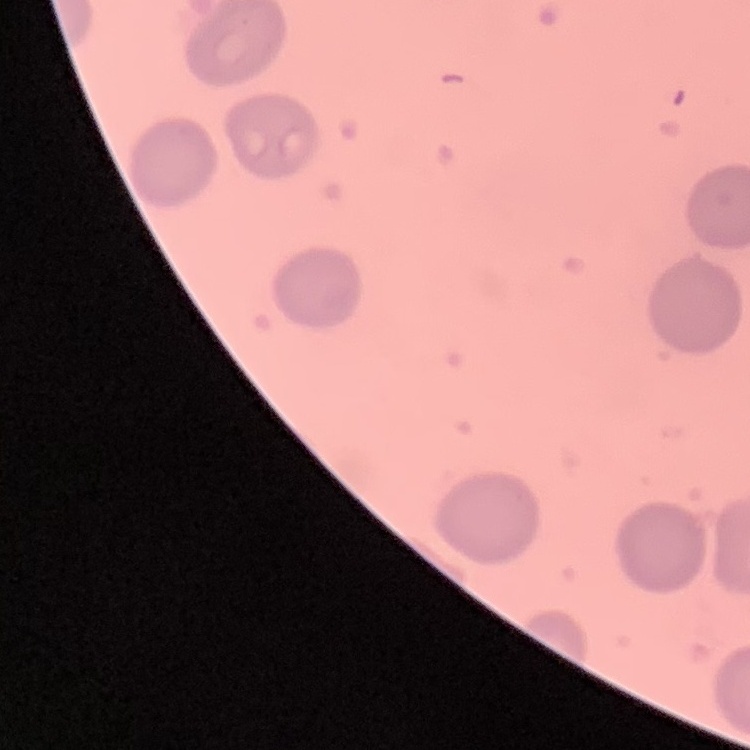
The erythrocytes exhibit no rouleaux formation. One tile cut from a larger photomicrograph. Thin peripheral smear. Stained with either Field's or Giemsa.